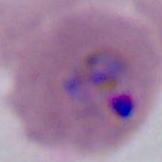
Summary:
  - Magnification: 400x or 1000x
  - Identification: Plasmodium
  - Modality: micrograph